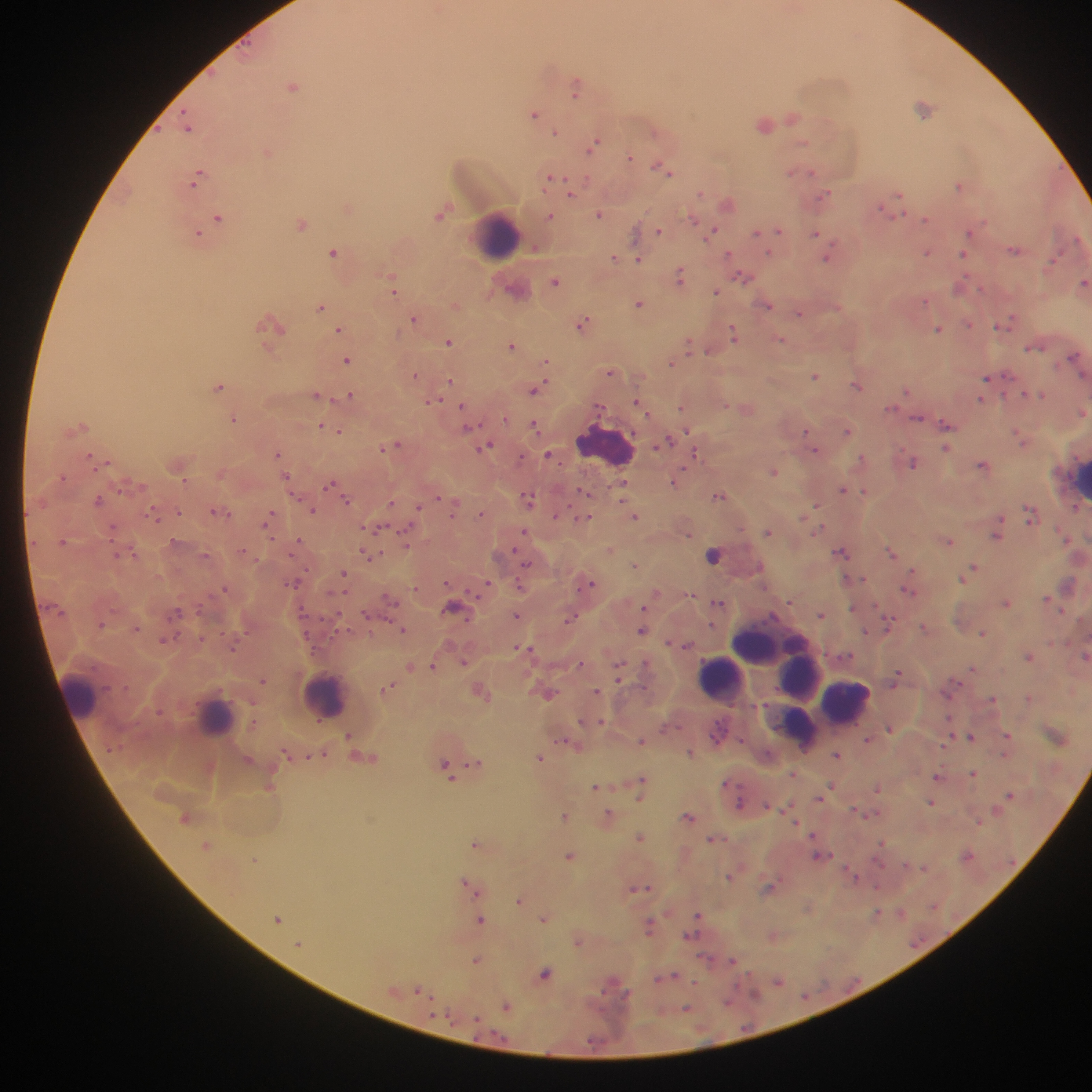

Approximate centers as x y in pixels.
Summary:
  - Plasmodium parasite locations: 293 86; 576 87; 924 108; 534 114; 793 118; 765 125; 188 127; 555 131; 594 143; 803 143; 268 153; 630 157; 662 169; 791 172; 811 172; 198 176; 551 177; 959 185; 571 191; 702 194; 899 194; 824 195; 728 203; 880 207; 892 207; 348 209; 599 214; 440 215; 551 216; 218 218; 693 219; 925 220; 301 224; 712 230; 778 230; 660 232; 756 232; 970 233; 197 234; 815 234; 1078 239; 534 249; 1015 249; 334 252; 927 252; 771 253; 728 254; 962 254; 827 257; 614 258; 638 259; 1053 259; 680 276; 742 277; 555 281; 1084 282; 959 286; 981 288; 394 289; 716 292; 925 301; 638 304; 767 305; 321 307; 799 313; 415 319; 581 323; 271 324; 1003 324; 969 325; 339 329; 937 329; 734 334; 781 340; 449 342; 511 345; 689 346; 1034 348; 709 351; 1073 356; 348 360; 546 361; 671 363; 610 373; 415 374; 815 376; 986 377; 450 381; 857 385; 218 386; 535 390; 907 390; 1024 394; 316 395; 1043 395; 349 396; 980 400; 433 402; 638 403; 463 405; 681 407; 646 411; 1082 413; 505 417; 233 418; 918 418; 320 425; 947 425; 82 427; 535 427; 469 428; 333 429; 340 431; 687 431; 846 431; 805 432; 1019 436; 667 441; 395 445; 486 446; 383 448; 947 449; 815 450; 278 454; 696 454; 550 455; 89 456; 520 458; 861 459; 108 461; 913 463; 982 464; 773 471; 286 476; 62 478; 184 479; 675 481; 329 484; 623 484; 842 489; 583 491; 865 492; 719 495; 438 497; 529 499; 98 500; 347 500; 390 504; 816 507; 418 508; 1076 508; 313 510; 216 511; 179 512; 454 512; 481 514; 556 515; 154 516; 1030 516; 270 517; 635 517; 584 518; 113 528; 524 532; 767 532; 689 534; 996 536; 299 540; 63 541; 949 541; 406 544; 610 549; 243 551; 841 552; 891 552; 135 554; 116 555; 205 555; 713 555; 367 556; 526 563; 635 565; 973 568; 912 570; 344 573; 969 573; 964 576; 846 579; 290 584; 590 584; 485 586; 521 586; 225 589; 908 590; 1047 598; 390 600; 718 603; 1006 603; 453 607; 852 607; 177 611; 821 615; 366 616; 516 616; 338 617; 570 618; 889 623; 102 625; 924 627; 136 628; 402 629; 641 631; 866 631; 983 633; 163 640; 686 646; 520 648; 530 649; 1030 656; 1085 656; 464 662; 579 663; 433 666; 410 667; 619 669; 973 669; 897 675; 263 681; 388 688; 597 691; 481 692; 549 693; 1029 697; 993 699; 601 722; 889 728; 348 735; 1008 735; 971 736; 866 739; 641 741; 567 742; 689 753; 837 754; 540 757; 475 763; 445 765; 792 774; 974 774; 936 776; 641 783; 832 785; 595 787; 878 788; 1009 794; 932 803; 740 804; 565 815; 608 815; 688 816; 978 822; 812 835; 641 838; 712 839; 475 843; 207 845; 967 855; 569 856; 818 857; 851 874; 730 876; 464 882; 470 887; 877 887; 641 888; 769 889; 476 892; 519 900; 901 912; 877 913; 278 919; 544 919; 480 920; 695 920; 648 927; 692 931; 578 942; 298 945; 475 960; 732 961; 545 974; 671 976; 661 979; 778 980; 419 989; 728 1000; 506 1007; 686 1008
  - Leukocyte locations: 498 235; 604 444; 1080 482; 767 639; 747 660; 791 669; 800 676; 719 678; 80 694; 325 695; 847 701; 215 715; 800 727
  - Field of view: single
  - Capture: mobile-phone photograph through a microscope
  - Country: Ghana
  - Preparation: thick blood film
  - Image size: 1092×1092 pixels